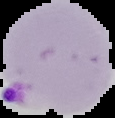
{
  "preparation": "thin blood film",
  "result": "malaria parasites identified",
  "image_type": "segmented cell region on a black background",
  "image_size": "115×118 pixels"
}